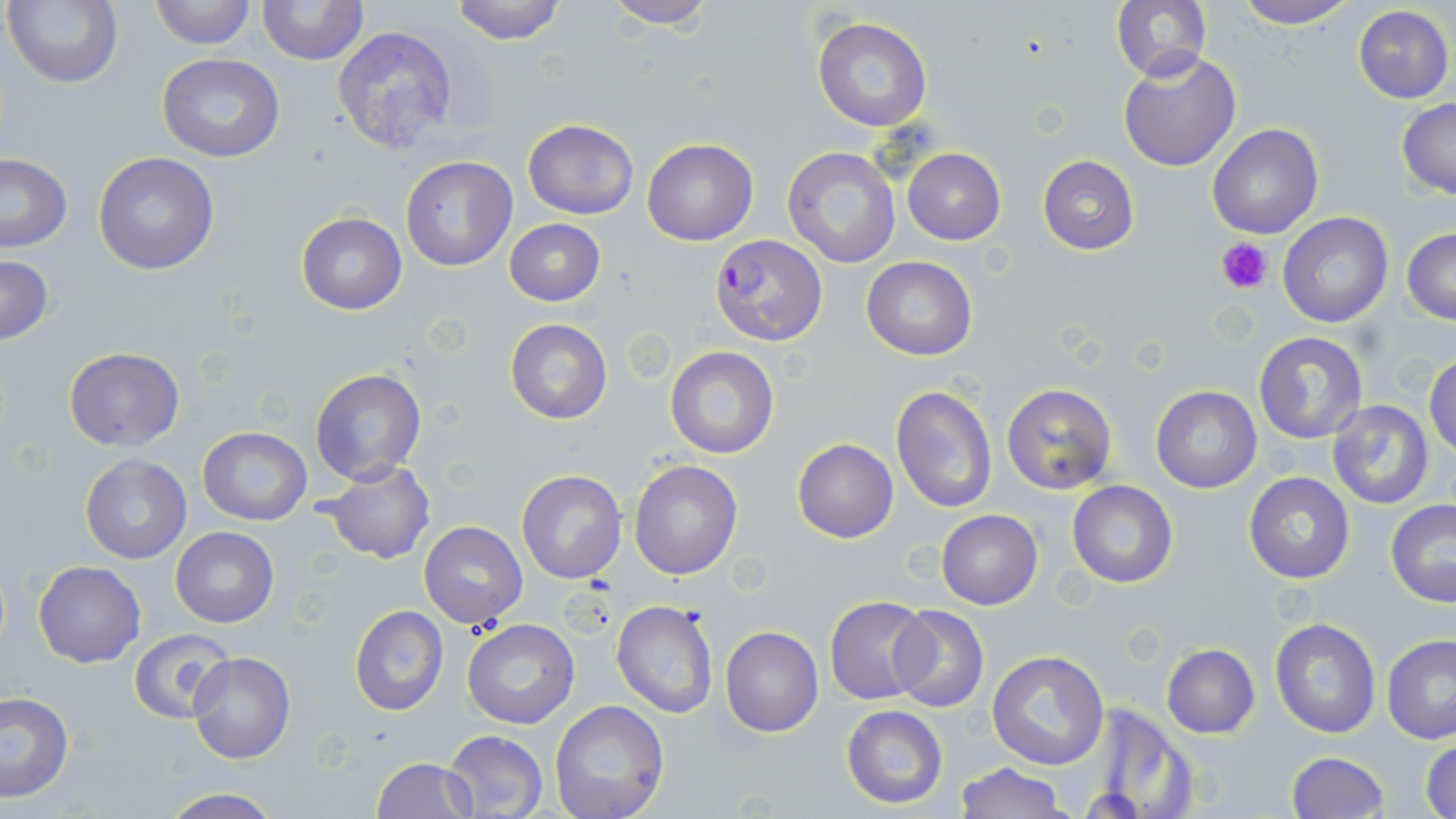

Approximate bounding boxes as (x1,y1)-(x2,y2) corner pairs in pixels. Platelet locations: (1215,237)-(1271,294). Plasmodium falciparum-infected red blood cell locations: (710,233)-(827,346). Uninfected red blood cell locations: (4,0)-(124,90), (148,0)-(255,49), (257,0)-(368,66), (449,0)-(569,44), (1111,0)-(1211,84), (1232,0)-(1360,28), (601,1)-(717,30), (1350,5)-(1454,104), (812,18)-(933,132), (330,24)-(461,154), (1118,50)-(1240,172), (157,54)-(286,163), (1396,98)-(1456,200), (522,118)-(641,220), (1207,124)-(1324,240), (643,138)-(759,245), (783,146)-(901,267), (902,147)-(1006,245), (0,153)-(73,254), (92,153)-(220,275), (1038,155)-(1139,255), (400,156)-(517,271), (1278,212)-(1394,328), (295,213)-(407,314), (504,218)-(605,306), (1402,227)-(1456,325), (0,254)-(54,347), (860,256)-(978,359), (505,319)-(612,423), (1252,330)-(1369,443), (664,346)-(780,460), (63,347)-(184,451), (1426,355)-(1456,457), (310,367)-(427,485), (1001,382)-(1117,494), (891,386)-(997,513), (1150,386)-(1261,493), (1325,399)-(1435,511), (197,427)-(312,526), (791,438)-(898,542), (78,453)-(193,564), (321,460)-(435,565), (629,460)-(743,581), (516,469)-(627,584), (1243,471)-(1356,585), (1067,481)-(1179,588), (1385,499)-(1456,606), (935,509)-(1042,611), (420,521)-(527,627), (171,527)-(278,627), (33,561)-(146,668), (824,595)-(933,704), (611,600)-(717,719), (889,605)-(989,712), (349,606)-(448,715), (1268,617)-(1381,739), (461,618)-(579,730), (720,626)-(822,738), (129,627)-(237,725), (1381,634)-(1456,745), (1160,643)-(1260,738), (987,649)-(1110,771), (187,651)-(296,764), (0,691)-(74,804), (550,700)-(670,819), (1084,702)-(1200,817), (841,704)-(948,810), (442,729)-(548,816), (1420,736)-(1456,819), (1287,751)-(1388,818), (371,758)-(478,818), (954,763)-(1069,818), (156,788)-(284,819). Slide-level diagnosis: Plasmodium falciparum. Captured at 1000x magnification. Thin blood smear. One field of a larger specimen. Image is 1456×819 pixels. May-Grünwald-Giemsa stain. Optical microscopy.